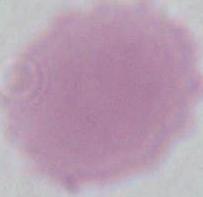

identification = erythrocyte
magnification = 1000x
modality = micrograph